Locate and identify every blood parasite.
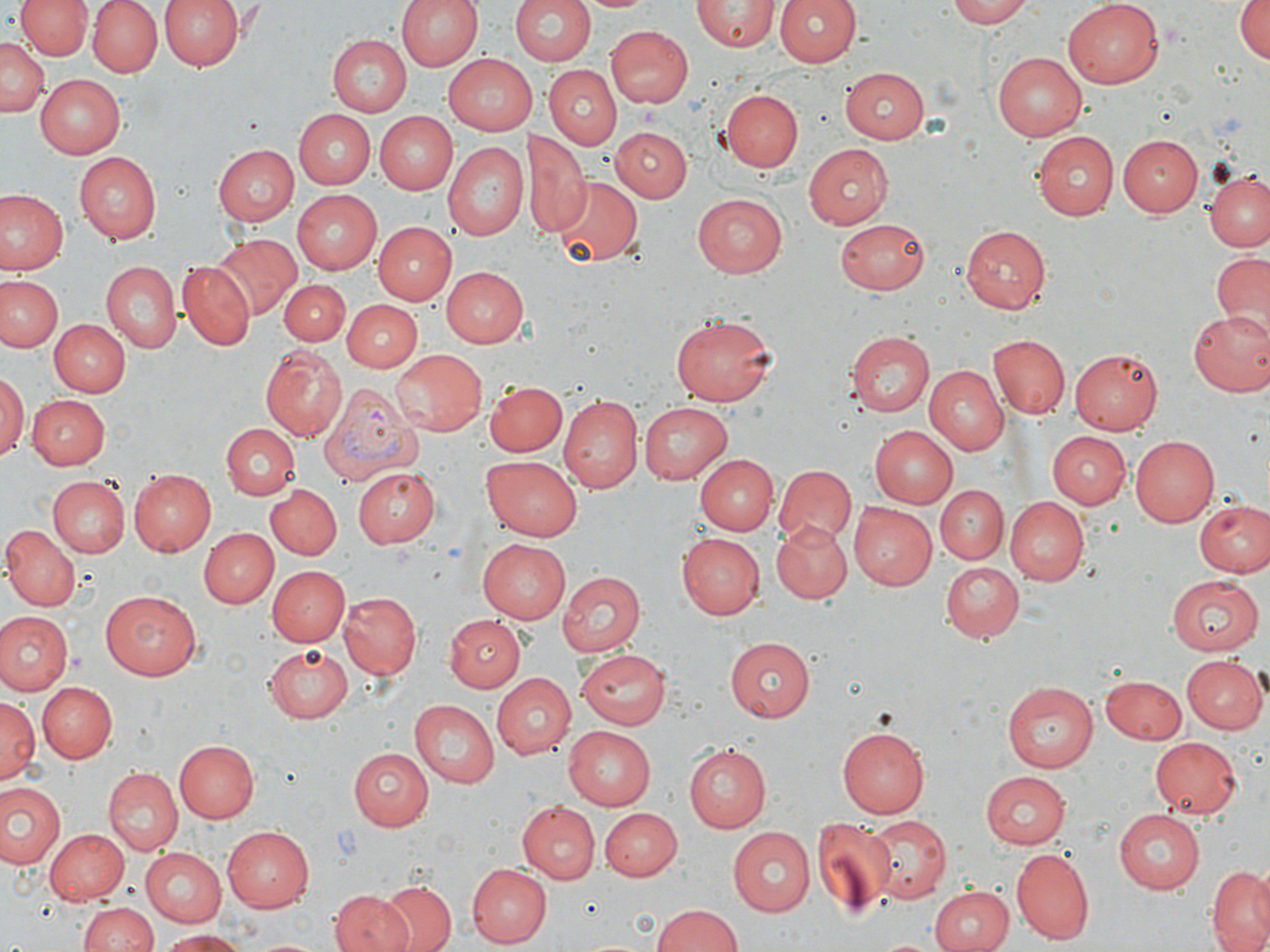

Approximate bounding boxes as (x1,y1)-(x2,y2) corner pairs in pixels.
Plasmodium vivax-infected red blood cells: (317,383)-(424,487).
No Plasmodium falciparum, Plasmodium ovale, Plasmodium malariae, Babesia divergens, or Trypanosoma brucei observed.

Uninfected red blood cell locations: (16,0)-(92,60), (85,0)-(161,77), (158,0)-(242,71), (395,0)-(480,72), (582,0)-(653,14), (775,0)-(859,68), (948,0)-(1041,27), (1064,0)-(1164,88), (1232,0)-(1269,66), (510,1)-(595,67), (692,2)-(777,53), (606,25)-(693,107), (328,34)-(411,117), (0,37)-(46,117), (992,52)-(1087,140), (442,54)-(535,136), (543,63)-(620,148), (839,65)-(928,144), (34,73)-(124,159), (720,90)-(803,172), (297,109)-(375,188), (375,112)-(458,193), (611,128)-(690,201), (528,131)-(587,239), (1030,131)-(1118,220), (1118,135)-(1203,216), (443,142)-(527,240), (803,142)-(892,229), (216,144)-(300,226), (74,152)-(162,244), (1206,172)-(1270,253), (552,178)-(643,265), (2,189)-(66,276), (291,190)-(381,273), (691,193)-(786,277), (835,218)-(930,295), (376,221)-(456,305), (960,225)-(1050,312), (212,233)-(301,318), (1213,251)-(1270,337), (100,262)-(180,353), (179,262)-(255,349), (441,266)-(527,345), (2,274)-(62,354), (277,279)-(349,344), (343,299)-(421,372), (1185,307)-(1270,394), (671,314)-(778,405), (49,318)-(128,396), (42,320)-(120,472), (849,330)-(937,416), (988,334)-(1070,420), (261,346)-(347,441), (1071,348)-(1163,433), (388,349)-(485,436), (923,366)-(1008,454), (0,373)-(26,462), (487,381)-(566,456), (29,396)-(109,468), (559,396)-(641,491), (639,402)-(734,484), (221,424)-(298,499), (869,425)-(959,506), (1045,431)-(1129,508), (1130,434)-(1222,526), (483,453)-(583,538), (696,454)-(776,534), (774,464)-(856,549), (352,467)-(441,547), (130,468)-(217,556), (46,475)-(129,558), (265,485)-(342,559), (935,485)-(1009,564), (1005,497)-(1091,587), (1193,500)-(1269,578), (849,502)-(938,591), (773,520)-(853,602), (1,526)-(79,611), (199,529)-(277,609), (676,533)-(765,619), (480,536)-(571,623), (940,562)-(1024,645), (267,566)-(350,647), (556,570)-(644,657), (1166,574)-(1263,656), (99,590)-(201,681), (341,593)-(420,677), (0,611)-(71,695), (444,616)-(524,691), (725,637)-(814,721), (264,644)-(353,720), (580,648)-(673,725), (1181,655)-(1266,734), (489,672)-(576,758), (1102,674)-(1189,742), (36,681)-(115,764), (1001,681)-(1099,773), (2,698)-(38,782), (408,699)-(500,787), (837,725)-(928,818), (563,726)-(656,809), (1149,738)-(1242,819), (175,740)-(258,822), (682,744)-(771,832), (349,747)-(434,831), (104,768)-(182,856), (980,771)-(1072,847), (0,782)-(66,872), (518,801)-(601,884), (602,807)-(682,880), (1110,807)-(1203,894), (864,815)-(951,902), (810,818)-(895,917), (222,825)-(314,911), (726,826)-(814,916), (44,828)-(127,904), (138,847)-(228,927), (1010,847)-(1095,943), (467,863)-(551,947), (1205,866)-(1270,952), (377,881)-(457,951), (931,884)-(1013,952), (332,891)-(413,952), (79,902)-(160,952), (654,904)-(743,952), (159,929)-(248,951). Slide-level diagnosis: Plasmodium vivax. Image is 1270×952 pixels. One field of a larger specimen. Thin blood film. Light microscopy. May-Grünwald-Giemsa stain. Captured at 1000x magnification.